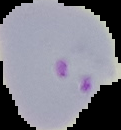
image type = cell region segmented out of the field of view; surrounding area masked to black
malaria status = parasitized
preparation = thin blood film
image size = 121×130 pixels